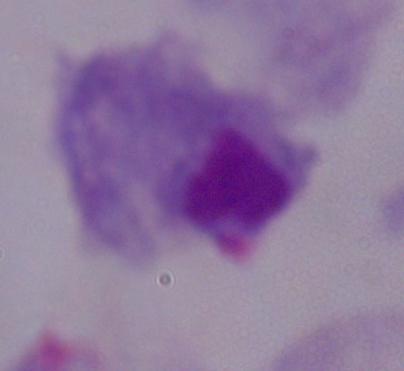
Photomicrograph. Captured at 1000x magnification. A trichomonad is seen.